Report the malaria status of this cell.
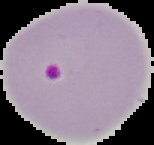

Parasitized.

Summary:
  - Image type: cell region segmented out of the field of view; surrounding area masked to black
  - Preparation: thin blood smear
  - Image size: 154×145 pixels